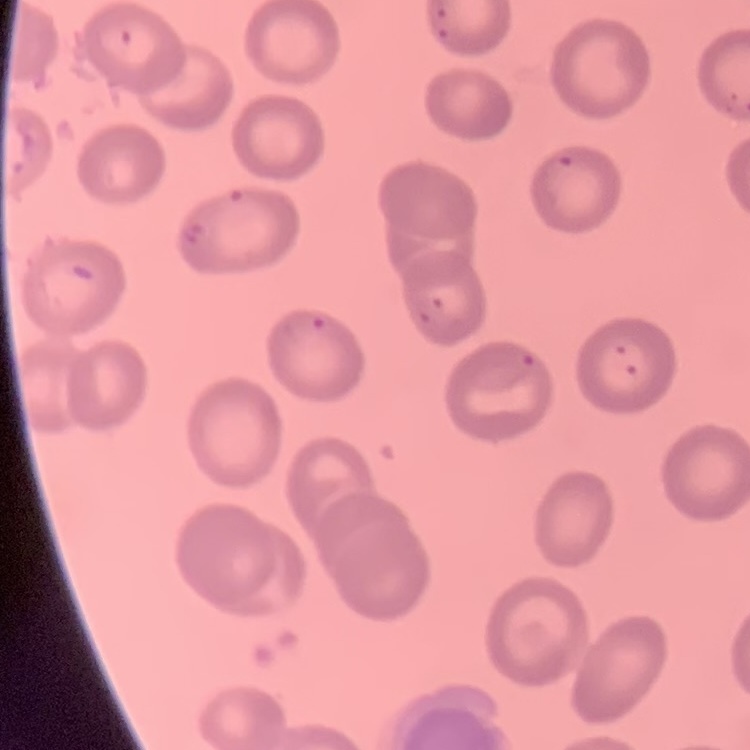

The red blood cells show no rouleaux formation. Square crop of a larger photomicrograph. Stained with either Field's or Giemsa. Thin peripheral smear.